Point out each Plasmodium parasite.
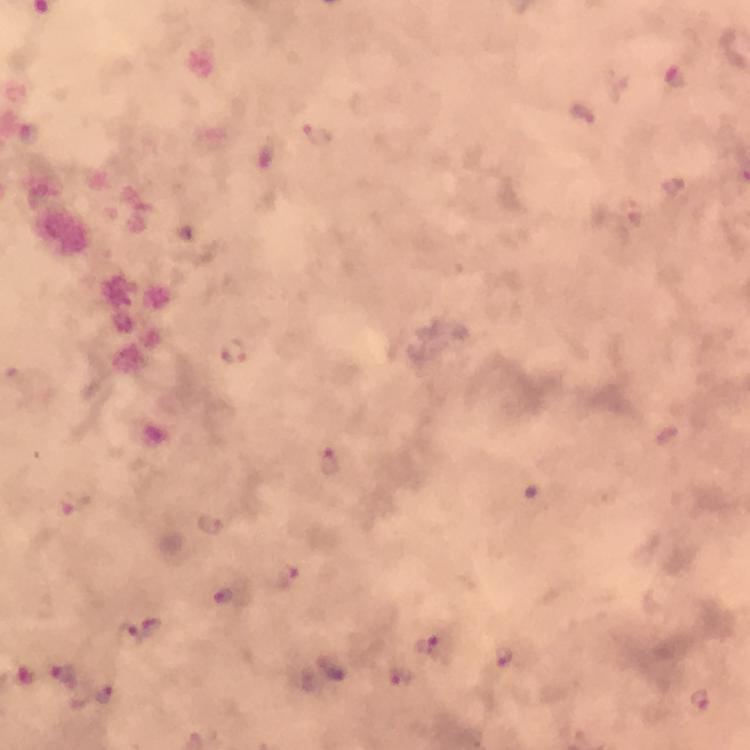

Approximate centers as [x, y] in pixels.
Plasmodium parasites: [675, 78], [321, 134], [235, 352], [331, 462], [210, 524], [288, 575], [143, 632], [432, 646], [503, 654], [334, 670], [24, 673], [65, 674], [398, 676], [700, 699].

Summary:
  - Context: from a malaria diagnostic workup
  - Capture: smartphone camera through the microscope
  - Preparation: thick smear
  - Image size: 750×750 pixels
  - Magnification: 100x
  - Cropped from: one field of view
  - Immersion oil: used
  - Stain: Giemsa